Identify the parasite.
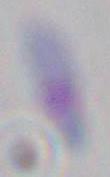

Toxoplasma gondii.

Summary:
  - Magnification: 1000x
  - Modality: photomicrograph